Identify the cell.
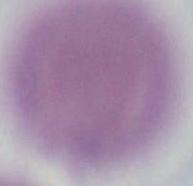

This is an erythrocyte.

Summary:
  - Modality: micrograph
  - Magnification: 1000x